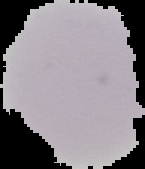 Result: no malaria parasites seen. From a thin blood film. Image is 145×169 pixels. The area outside the segmented cell region is set to black.